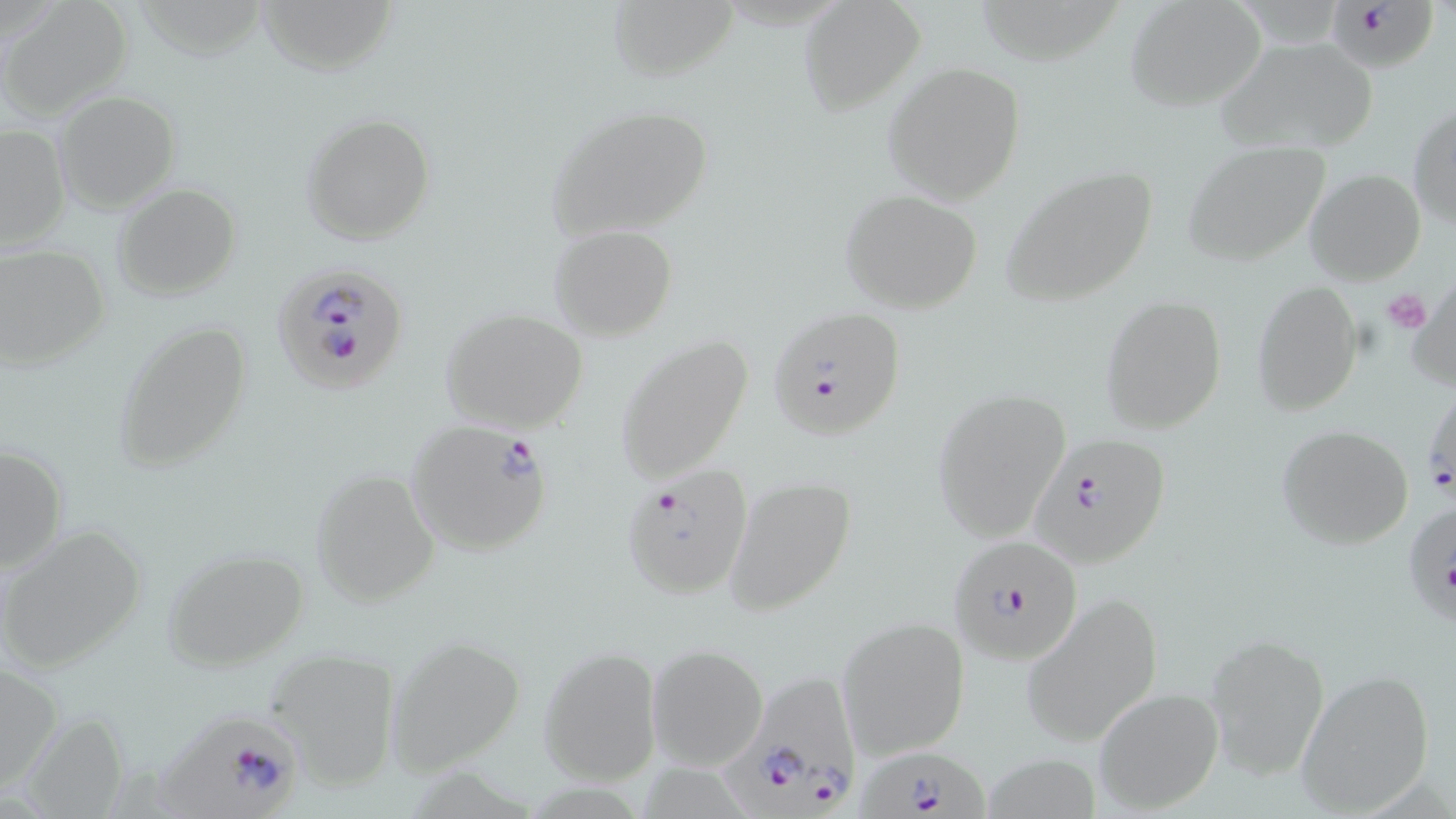
Approximate bounding boxes as (x1, y1, x2, y2) in pixels. Plasmodium falciparum-infected red blood cell locations: (1326, 0, 1437, 72), (274, 262, 409, 395), (767, 308, 905, 441), (1423, 379, 1455, 506), (405, 419, 554, 557), (1029, 432, 1175, 568), (621, 465, 754, 600), (1401, 501, 1456, 634), (947, 534, 1085, 666), (712, 670, 863, 819), (142, 701, 314, 819), (863, 748, 988, 819). Uninfected red blood cell locations: (1, 0, 135, 118), (254, 0, 400, 75), (798, 0, 924, 112), (603, 1, 736, 81), (1125, 1, 1266, 112), (972, 2, 1121, 71), (1216, 37, 1379, 156), (883, 62, 1028, 203), (54, 91, 180, 213), (1408, 102, 1455, 230), (542, 103, 716, 241), (300, 112, 437, 246), (0, 123, 71, 249), (1182, 141, 1331, 267), (1001, 164, 1160, 310), (1304, 169, 1426, 285), (113, 183, 241, 300), (841, 190, 984, 315), (547, 225, 676, 341), (0, 244, 111, 371), (1408, 275, 1455, 397), (1250, 282, 1363, 415), (1100, 295, 1226, 434), (440, 307, 590, 433), (111, 317, 254, 475), (613, 336, 754, 484), (933, 387, 1069, 539), (1277, 424, 1415, 550), (1, 443, 69, 572), (310, 468, 440, 606), (723, 475, 857, 616), (0, 524, 148, 673), (161, 546, 311, 671), (1019, 592, 1164, 747), (836, 617, 970, 759), (1204, 634, 1328, 777), (385, 635, 524, 774), (647, 644, 769, 771), (263, 647, 403, 789), (539, 647, 661, 787), (0, 662, 60, 795), (1295, 669, 1435, 815), (1092, 687, 1223, 814). Platelet locations: (1381, 288, 1432, 333). Slide-level diagnosis: Plasmodium falciparum. One field of a larger specimen. Thin blood smear. Light microscopy. 1000x magnification. Image is 1456×819 pixels. May-Grünwald-Giemsa stain.